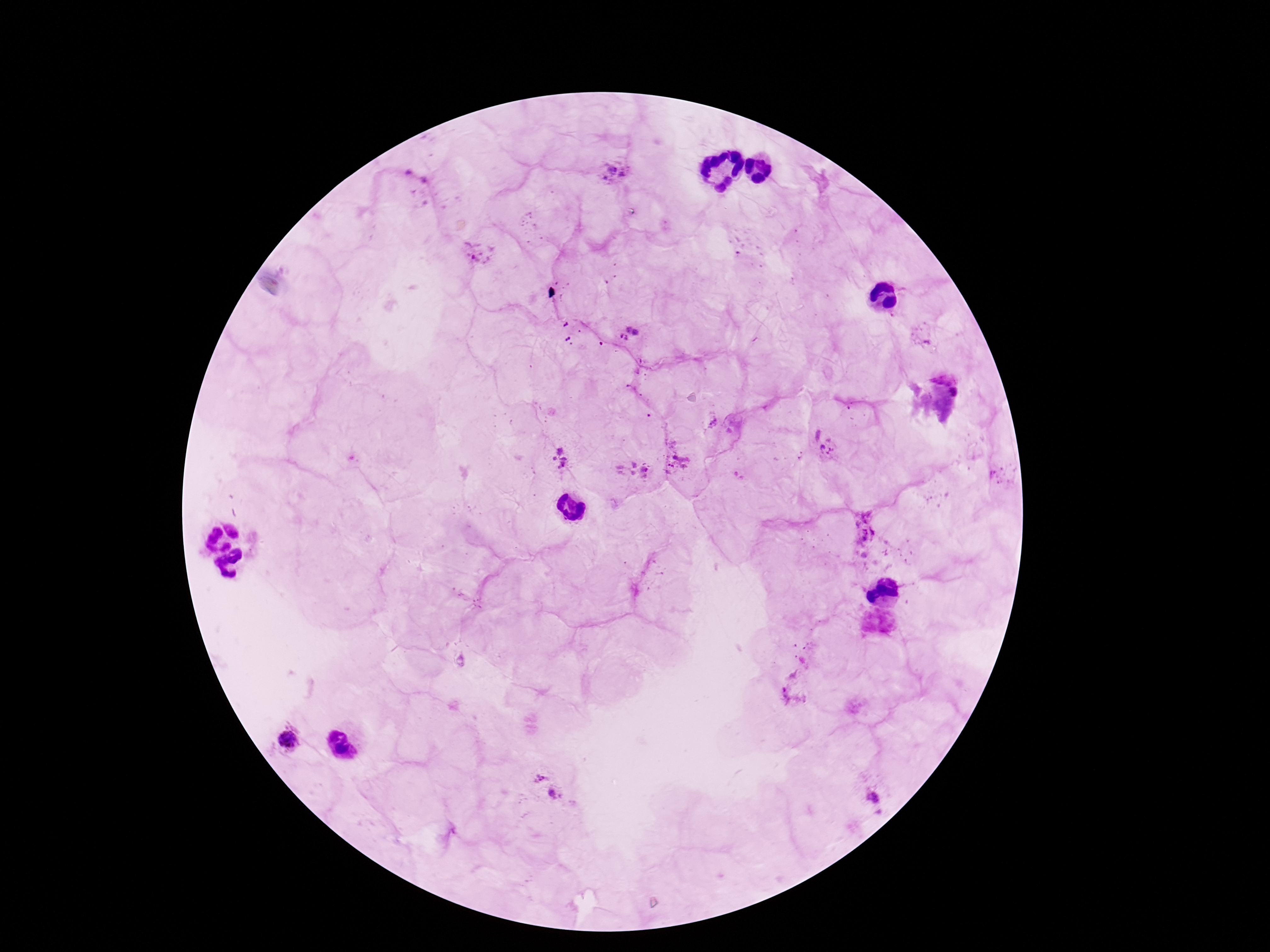
Plasmodium parasite locations = approximate centers as {x, y} in pixels: {614, 170}, {479, 255}, {629, 333}, {823, 443}, {560, 458}, {676, 460}, {633, 469}, {865, 533}, {792, 693}, {288, 740}, {544, 784}, {874, 796}
image size = 1270×952 pixels
magnification = 100x
preparation = thick peripheral-blood smear
patient malaria status = infected
capture = smartphone camera through the microscope eyepiece
stain = Giemsa
field of view = one from this slide